Describe the morphology of the red blood cells.
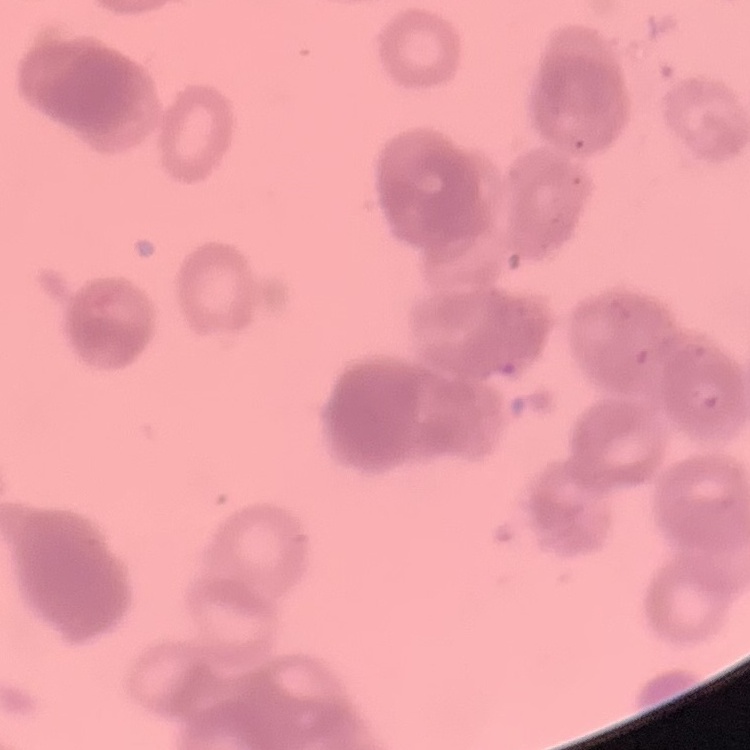
Rouleaux formation.

preparation = thin blood film
image type = one tile cut from a larger photomicrograph
stain = Field's or Giemsa